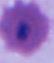
identification: Plasmodium
modality: photomicrograph
magnification: 400x or 1000x